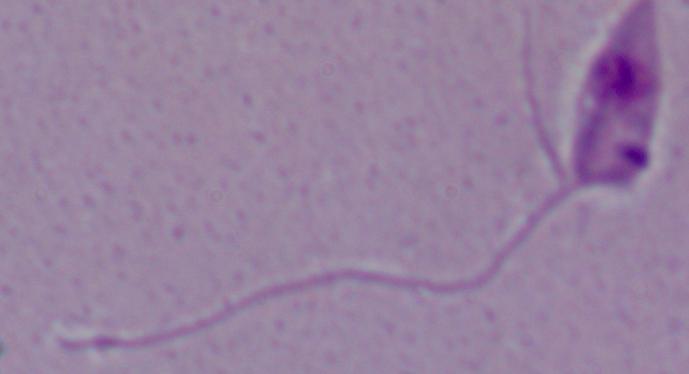
{
  "modality": "micrograph",
  "identification": "Leishmania",
  "magnification": "1000x"
}